Locate every leukocyte (white blood cell).
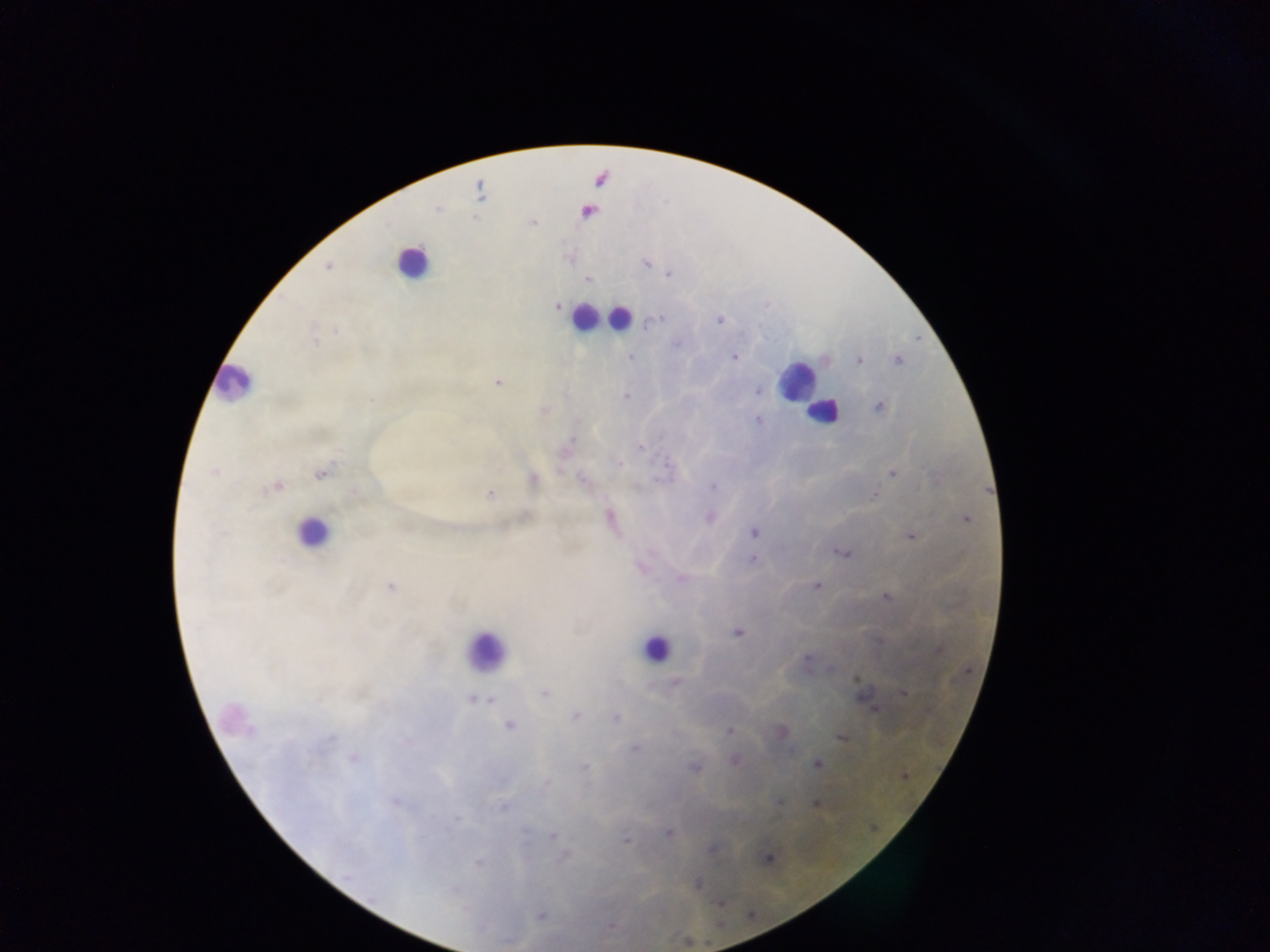
Approximate centers as x y in pixels.
Leukocytes: 411 262; 589 318; 618 318; 796 381; 233 384; 823 412; 312 533; 655 648; 485 651.

country = Ghana
preparation = thick blood smear
Plasmodium parasite locations = approximate centers as x y in pixels: 600 179; 479 191; 438 209; 586 212; 645 263; 327 267; 669 273; 588 278; 558 306; 718 320; 650 322; 337 330; 314 341; 734 356; 630 357; 858 360; 898 360; 497 382; 757 391; 626 396; 879 407; 543 410; 757 420; 573 440; 640 447; 617 462; 214 472; 892 472; 320 473; 532 479; 584 480; 276 486; 713 486; 490 494; 875 495; 609 518; 710 518; 964 518; 754 533; 910 535; 841 552; 753 560; 641 566; 681 578; 816 585; 390 587; 886 596; 737 632; 938 648; 675 682; 544 693; 904 693; 475 699; 488 699; 873 707; 576 715; 615 718; 509 724; 782 731; 730 732; 841 737; 635 748; 354 758; 734 760; 818 763; 583 767; 695 768; 905 775; 779 803; 814 803; 503 805; 668 833; 552 835; 625 840; 711 850; 563 858; 767 858; 480 863; 696 883; 718 902; 541 914
image size = 1270×952 pixels
field of view = single
capture = mobile-phone photograph through a microscope